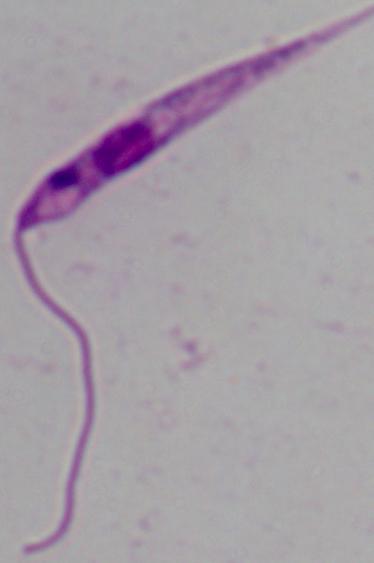

Summary:
  - Magnification: 1000x
  - Identification: Leishmania
  - Modality: micrograph